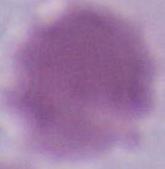
Summary:
  - Modality: photomicrograph
  - Identification: red blood cell
  - Magnification: 1000x